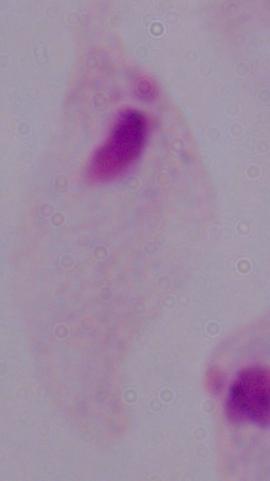

identification = trichomonad
magnification = 1000x
modality = micrograph